Point out each Plasmodium parasite.
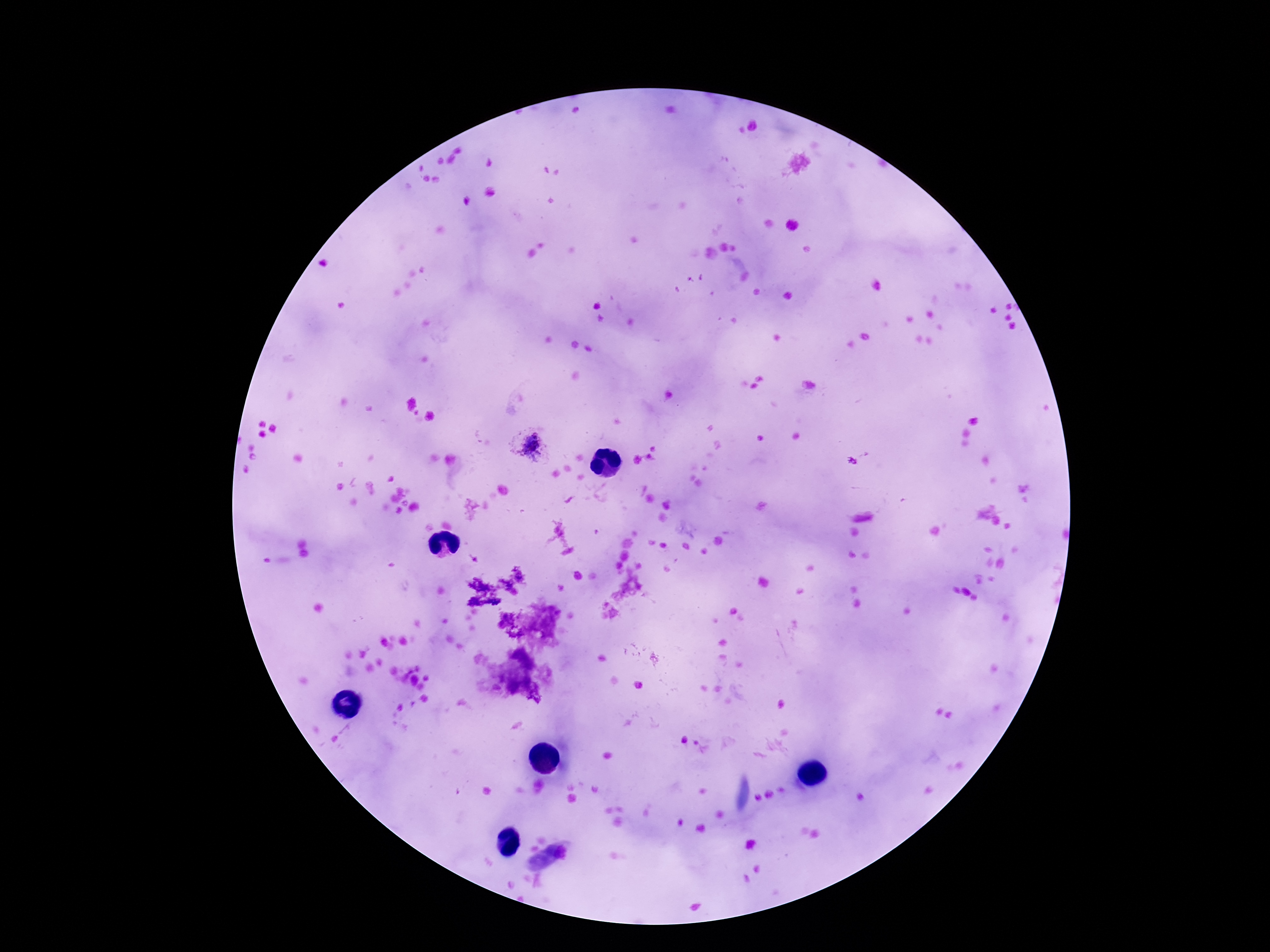
Approximate centers as {x, y} in pixels.
Plasmodium parasites: {530, 445}.

Summary:
  - Image size: 1270×952 pixels
  - Patient malaria status: positive
  - Capture: smartphone camera through the microscope eyepiece
  - Preparation: thick blood smear
  - Magnification: 100x
  - Field of view: one from this slide
  - Stain: Giemsa